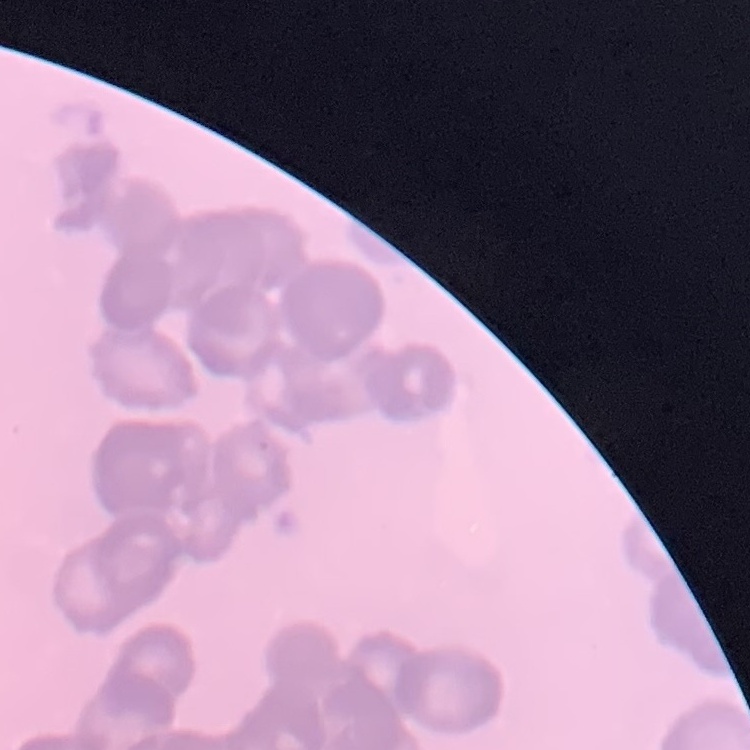 The erythrocytes exhibit rouleaux formation. Stained with either Field's or Giemsa. Thin blood film. Square crop of a larger photomicrograph.